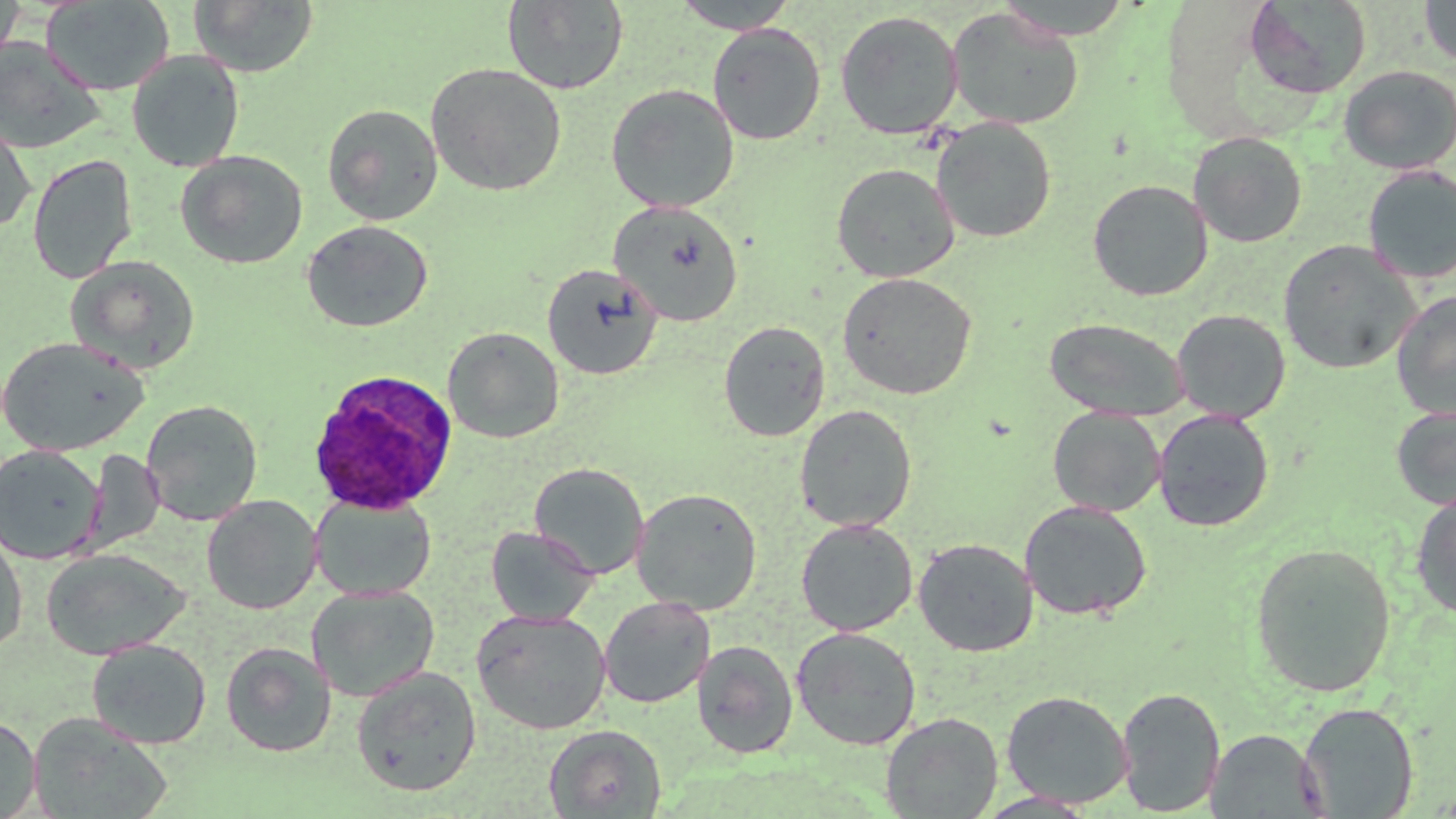

{
  "slide_level_diagnosis": "Plasmodium ovale",
  "preparation": "thin blood smear",
  "field_of_view": "one of a larger specimen",
  "stain": "May-Grünwald-Giemsa",
  "plasmodium_ovale_infected_red_blood_cell_locations": "approximate bounding boxes as (x1,y1)-(x2,y2) corner pairs in pixels: (307,368)-(459,515)",
  "magnification": "1000x",
  "modality": "light microscopy",
  "uninfected_red_blood_cell_locations": "approximate bounding boxes as (x1,y1)-(x2,y2) corner pairs in pixels: (0,0)-(25,70), (188,0)-(319,77), (673,0)-(800,33), (995,0)-(1136,40), (41,1)-(174,95), (502,1)-(629,94), (1244,1)-(1371,99), (1420,1)-(1455,68), (946,7)-(1084,130), (835,9)-(963,140), (707,23)-(826,145), (0,37)-(105,154), (127,50)-(245,172), (425,63)-(568,197), (1338,65)-(1456,175), (606,83)-(740,213), (322,103)-(443,225), (0,114)-(36,234), (931,117)-(1057,243), (1188,131)-(1308,248), (175,150)-(308,269), (27,153)-(138,284), (831,163)-(959,283), (1362,165)-(1456,284), (1088,179)-(1213,301), (608,201)-(743,326), (301,219)-(432,333), (1277,239)-(1421,374), (66,254)-(201,374), (542,263)-(663,380), (837,271)-(977,400), (1391,290)-(1456,418), (1172,308)-(1291,423), (1044,317)-(1189,421), (718,321)-(831,442), (442,326)-(564,443), (0,336)-(149,457), (140,400)-(263,526), (794,404)-(917,532), (1390,404)-(1456,509), (1048,406)-(1165,516), (1153,409)-(1274,532), (1,444)-(105,564), (83,449)-(164,555), (529,462)-(649,580), (631,487)-(763,615), (1410,490)-(1456,619), (310,493)-(436,601), (202,495)-(322,615), (1019,500)-(1153,621), (796,519)-(918,636), (486,525)-(599,627), (0,528)-(28,655), (913,537)-(1038,657), (1250,541)-(1397,698), (40,548)-(189,660), (306,585)-(440,702), (598,596)-(715,709), (472,608)-(610,735), (792,626)-(921,750), (87,638)-(211,749), (692,639)-(798,758), (220,641)-(336,757), (351,666)-(482,796), (1116,686)-(1226,816), (1002,690)-(1133,808), (1298,702)-(1418,818), (27,712)-(174,819), (881,712)-(1003,818), (0,714)-(41,818), (544,724)-(667,817), (1206,729)-(1326,817), (974,791)-(1099,817)",
  "image_size": "1456×819 pixels"
}